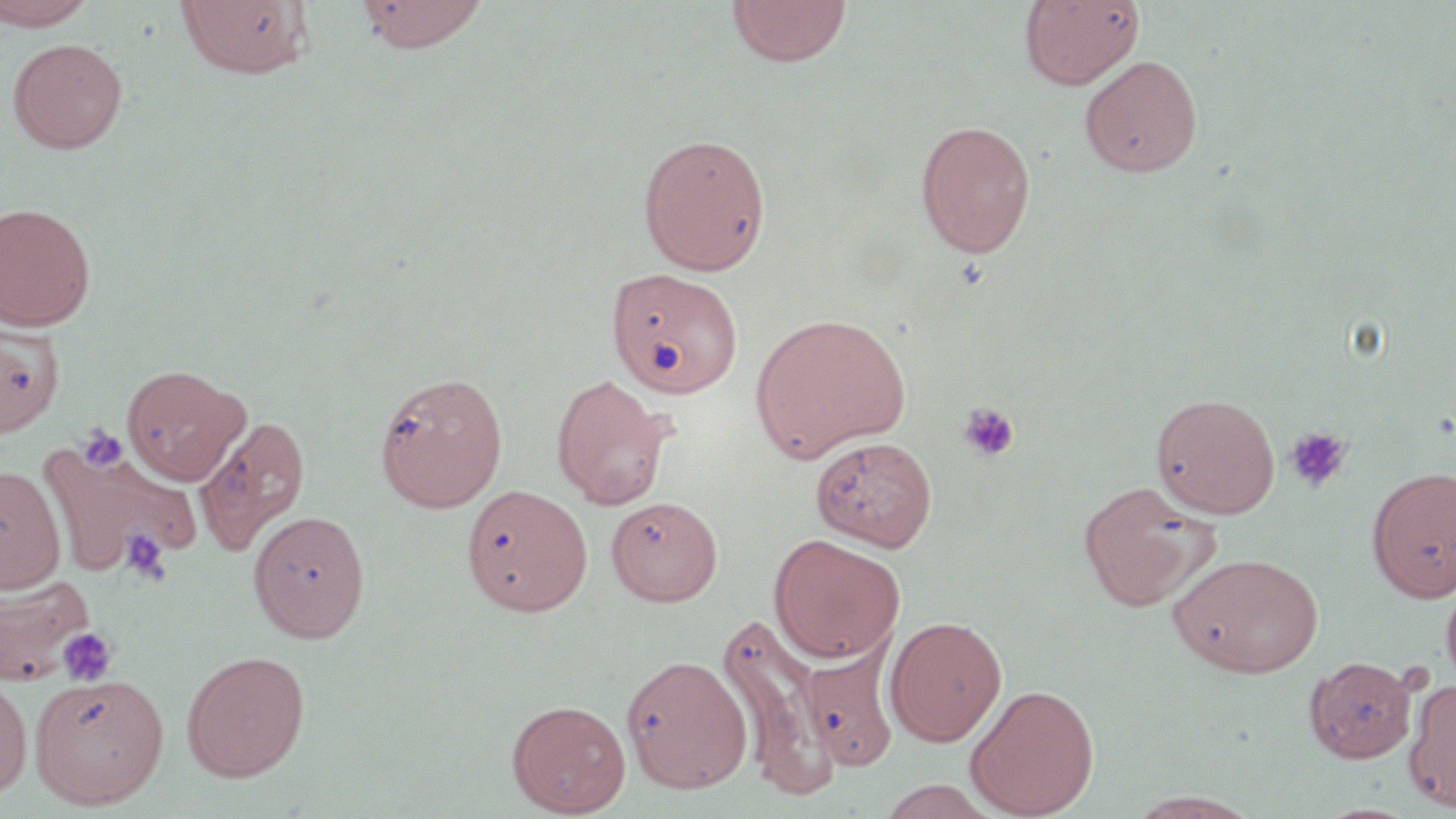
Summary:
  - Coordinate format: approximate bounding boxes as named x1/y1/x2/y2 corners in pixels
  - Platelet locations: (x1=958, y1=401, x2=1020, y2=463), (x1=78, y1=426, x2=127, y2=473), (x1=1284, y1=427, x2=1352, y2=492), (x1=120, y1=529, x2=171, y2=586), (x1=57, y1=627, x2=117, y2=686)
  - Uninfected red blood cell locations: (x1=0, y1=0, x2=97, y2=30), (x1=354, y1=0, x2=489, y2=53), (x1=1020, y1=0, x2=1145, y2=90), (x1=175, y1=1, x2=313, y2=79), (x1=725, y1=1, x2=851, y2=68), (x1=6, y1=38, x2=128, y2=154), (x1=1078, y1=54, x2=1203, y2=178), (x1=915, y1=119, x2=1036, y2=258), (x1=637, y1=132, x2=771, y2=275), (x1=0, y1=202, x2=97, y2=331), (x1=607, y1=266, x2=744, y2=397), (x1=750, y1=312, x2=911, y2=462), (x1=0, y1=322, x2=63, y2=436), (x1=122, y1=364, x2=251, y2=485), (x1=375, y1=371, x2=508, y2=512), (x1=551, y1=373, x2=675, y2=510), (x1=1151, y1=392, x2=1280, y2=518), (x1=194, y1=414, x2=310, y2=558), (x1=810, y1=435, x2=937, y2=551), (x1=43, y1=447, x2=197, y2=576), (x1=0, y1=464, x2=66, y2=594), (x1=1366, y1=466, x2=1456, y2=602), (x1=1077, y1=480, x2=1216, y2=611), (x1=462, y1=484, x2=593, y2=616), (x1=606, y1=496, x2=722, y2=606), (x1=248, y1=509, x2=370, y2=643), (x1=769, y1=534, x2=906, y2=664), (x1=1168, y1=551, x2=1324, y2=677), (x1=0, y1=571, x2=95, y2=686), (x1=1441, y1=576, x2=1456, y2=693), (x1=718, y1=614, x2=836, y2=796), (x1=884, y1=615, x2=1007, y2=746), (x1=799, y1=648, x2=898, y2=771), (x1=181, y1=650, x2=311, y2=782), (x1=622, y1=654, x2=753, y2=793), (x1=1304, y1=656, x2=1419, y2=763), (x1=0, y1=671, x2=33, y2=801), (x1=29, y1=672, x2=169, y2=809), (x1=1403, y1=679, x2=1456, y2=812), (x1=965, y1=683, x2=1100, y2=818), (x1=506, y1=699, x2=631, y2=817), (x1=1128, y1=790, x2=1258, y2=818)
  - Slide-level diagnosis: negative for blood parasites
  - Magnification: 1000x
  - Field of view: single
  - Stain: May-Grünwald-Giemsa
  - Image size: 1456×819 pixels
  - Modality: light microscopy
  - Preparation: thin blood film